Report the malaria status of this cell.
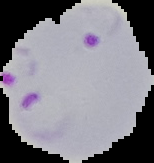

Parasitized.

Summary:
  - Image type: segmented cell region on a black background
  - Preparation: thin blood film
  - Image size: 154×163 pixels